Locate every Plasmodium parasite.
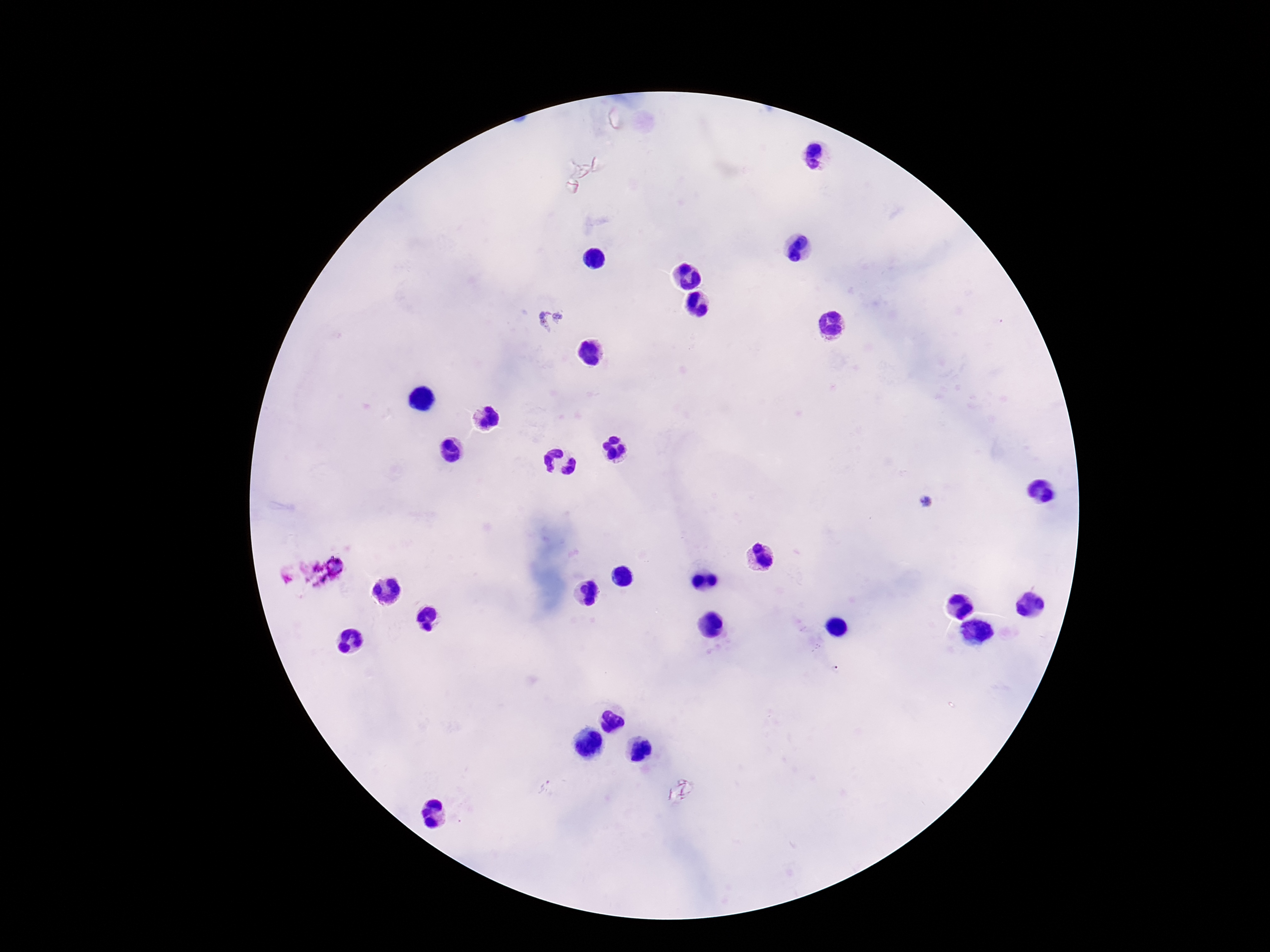

Approximate centers as [x, y] in pixels.
Plasmodium parasites: [549, 319], [927, 501].

magnification: 100x
capture: smartphone camera through the microscope eyepiece
patient_malaria_status: positive
stain: Giemsa
field_of_view: one from this slide
preparation: thick blood smear
image_size: 1270×952 pixels